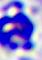
Summary:
  - Identification: white blood cell
  - Modality: photomicrograph
  - Magnification: 400x